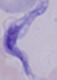

A trypanosome is shown. Micrograph. Captured at 1000x magnification.